Assess this cell for malaria.
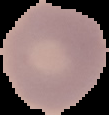

Uninfected.

image size = 109×115 pixels
preparation = thin blood film
image type = cell region segmented out of the field of view; surrounding area masked to black